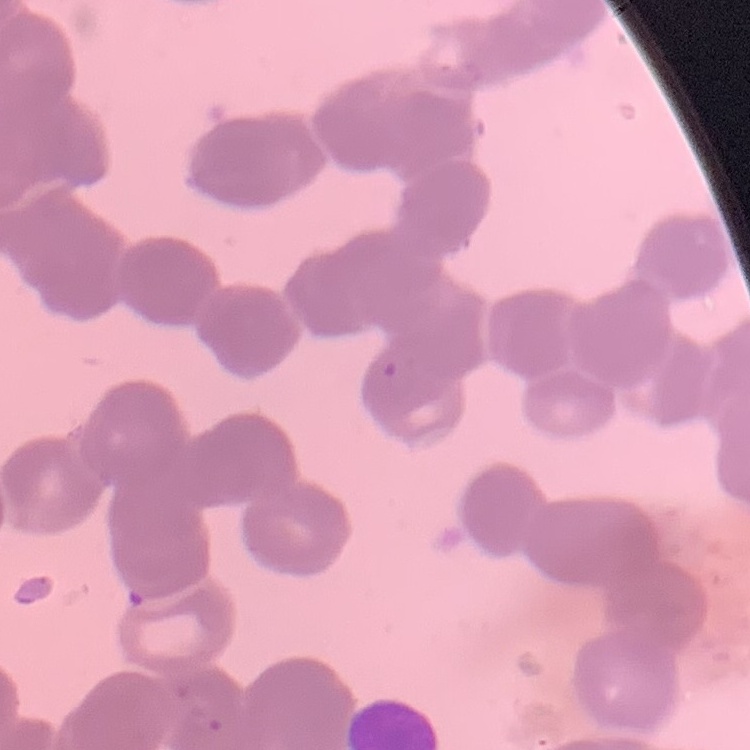 The erythrocytes show rouleaux formation. Square crop of a larger photomicrograph. Thin peripheral smear. Field's or Giemsa stain.